Identify the blood parasite species.
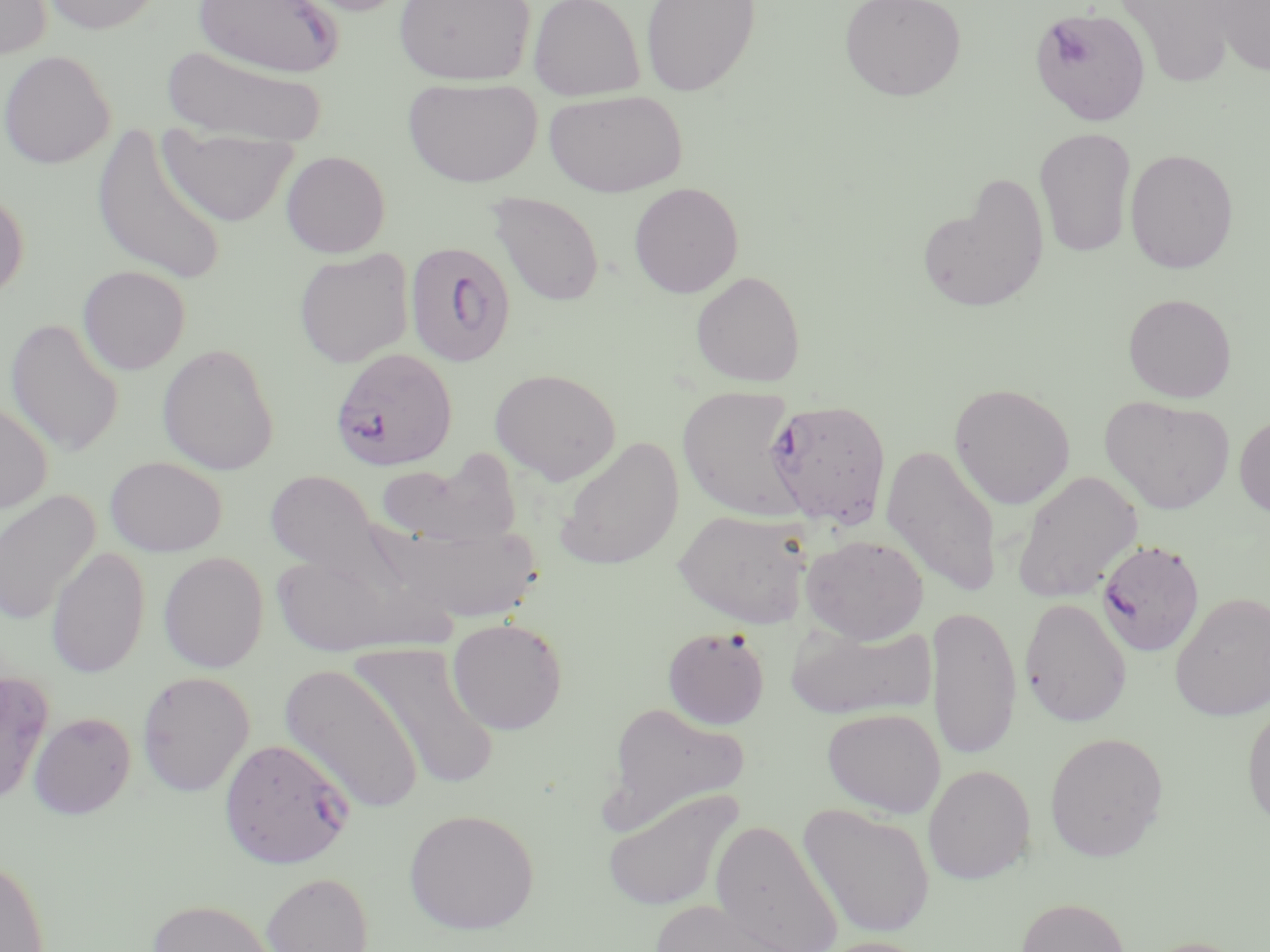
Plasmodium falciparum.

magnification = 1000x
modality = optical microscopy
uninfected red blood cell locations = approximate bounding boxes as [x1, y1, x2, y2] in pixels: [0, 0, 54, 62], [36, 0, 165, 35], [193, 0, 345, 77], [285, 0, 416, 17], [393, 0, 535, 85], [528, 0, 645, 100], [640, 0, 761, 96], [839, 0, 967, 101], [1117, 0, 1242, 86], [1210, 1, 1270, 78], [162, 45, 326, 145], [0, 49, 116, 169], [402, 78, 542, 187], [543, 89, 687, 197], [91, 124, 228, 285], [1034, 128, 1137, 257], [159, 131, 298, 227], [1125, 148, 1239, 273], [280, 150, 391, 258], [918, 179, 1049, 315], [628, 182, 744, 298], [0, 186, 30, 302], [487, 191, 605, 307], [294, 248, 415, 368], [77, 265, 191, 375], [690, 270, 806, 387], [1122, 293, 1237, 402], [4, 318, 124, 458], [157, 342, 280, 476], [489, 368, 622, 485], [949, 382, 1075, 510], [677, 385, 805, 521], [1099, 395, 1235, 514], [0, 399, 53, 514], [1234, 411, 1270, 519], [554, 437, 684, 570], [881, 443, 1002, 597], [377, 450, 522, 549], [105, 456, 227, 557], [265, 470, 386, 577], [1011, 470, 1143, 602], [0, 490, 101, 627], [673, 508, 813, 627], [390, 523, 543, 622], [801, 534, 929, 643], [46, 546, 150, 679], [271, 549, 405, 657], [158, 551, 269, 673], [1169, 591, 1270, 721], [1019, 597, 1132, 728], [927, 605, 1022, 762], [446, 617, 568, 734], [786, 622, 937, 720], [661, 626, 771, 729], [351, 642, 500, 793], [279, 661, 425, 816], [0, 669, 51, 807], [135, 670, 255, 797], [602, 701, 752, 832], [1242, 701, 1270, 833], [822, 707, 946, 818], [28, 712, 136, 819], [1044, 731, 1169, 861], [923, 764, 1035, 884], [602, 788, 743, 912], [799, 804, 936, 939], [404, 808, 539, 934], [711, 821, 842, 952], [0, 855, 51, 952], [261, 872, 373, 952], [1016, 897, 1131, 952], [147, 898, 276, 952], [649, 899, 803, 952], [810, 936, 934, 952], [1137, 936, 1255, 952]
Plasmodium falciparum-infected red blood cell locations = approximate bounding boxes as [x1, y1, x2, y2] in pixels: [1030, 7, 1152, 126], [404, 241, 517, 368], [329, 348, 458, 472], [764, 398, 892, 529], [1096, 539, 1205, 657], [219, 737, 354, 869]
stain = May-Grünwald-Giemsa
field of view = one of a larger specimen
image size = 1270×952 pixels
preparation = thin blood smear